Assess the morphology of the erythrocytes.
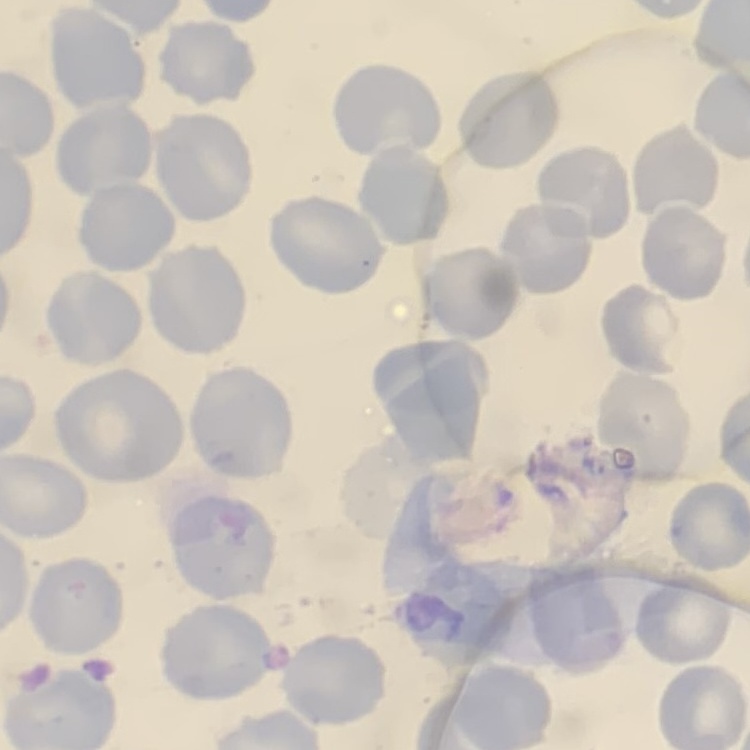

They show no rouleaux formation.

Summary:
  - Image type: one tile cut from a larger photomicrograph
  - Stain: Field's or Giemsa
  - Preparation: thin blood film